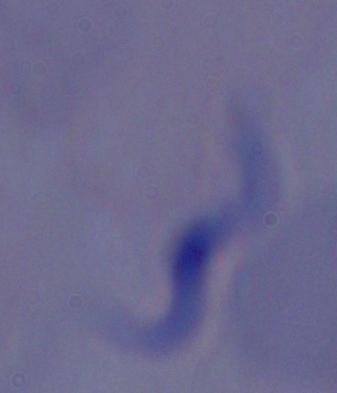

Summary:
  - Magnification: 1000x
  - Identification: trypanosome
  - Modality: photomicrograph